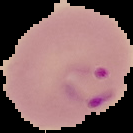 Segmented cell region on a black background. Image is 133×133 pixels. Result: Plasmodium parasites identified. From a thin blood film.